Report the malaria status of this cell.
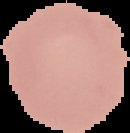
Uninfected.

image type = cell region segmented out of the field of view; surrounding area masked to black
preparation = thin blood film
image size = 130×133 pixels